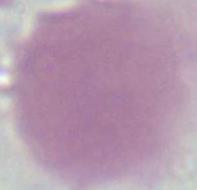

modality = photomicrograph
magnification = 1000x
identification = red blood cell